Assess this cell for malaria.
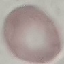
Uninfected.

preparation = thin blood smear
stain = Giemsa
capture = smartphone through the microscope eyepiece
image type = cell patch, automatically extracted from a larger field of view and resized to 64 × 64 pixels